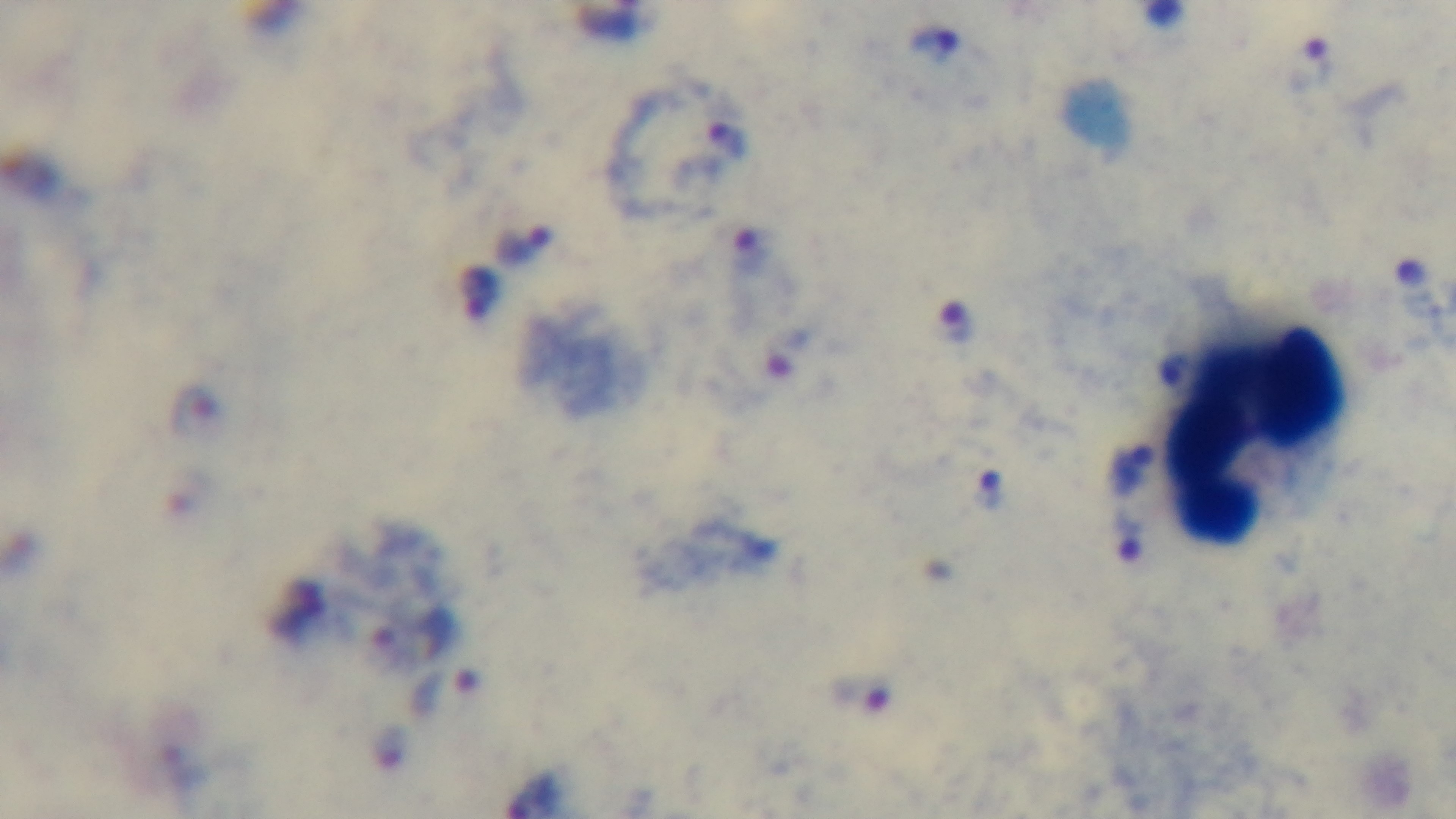
Summary:
  - Field of view: one from the slide
  - Objective: 100x oil immersion
  - Malaria status: positive
  - Stain: Giemsa
  - Modality: light microscopy
  - Capture: mounted 4K digital camera
  - Preparation: thick smear